Locate every Plasmodium falciparum-infected red blood cell.
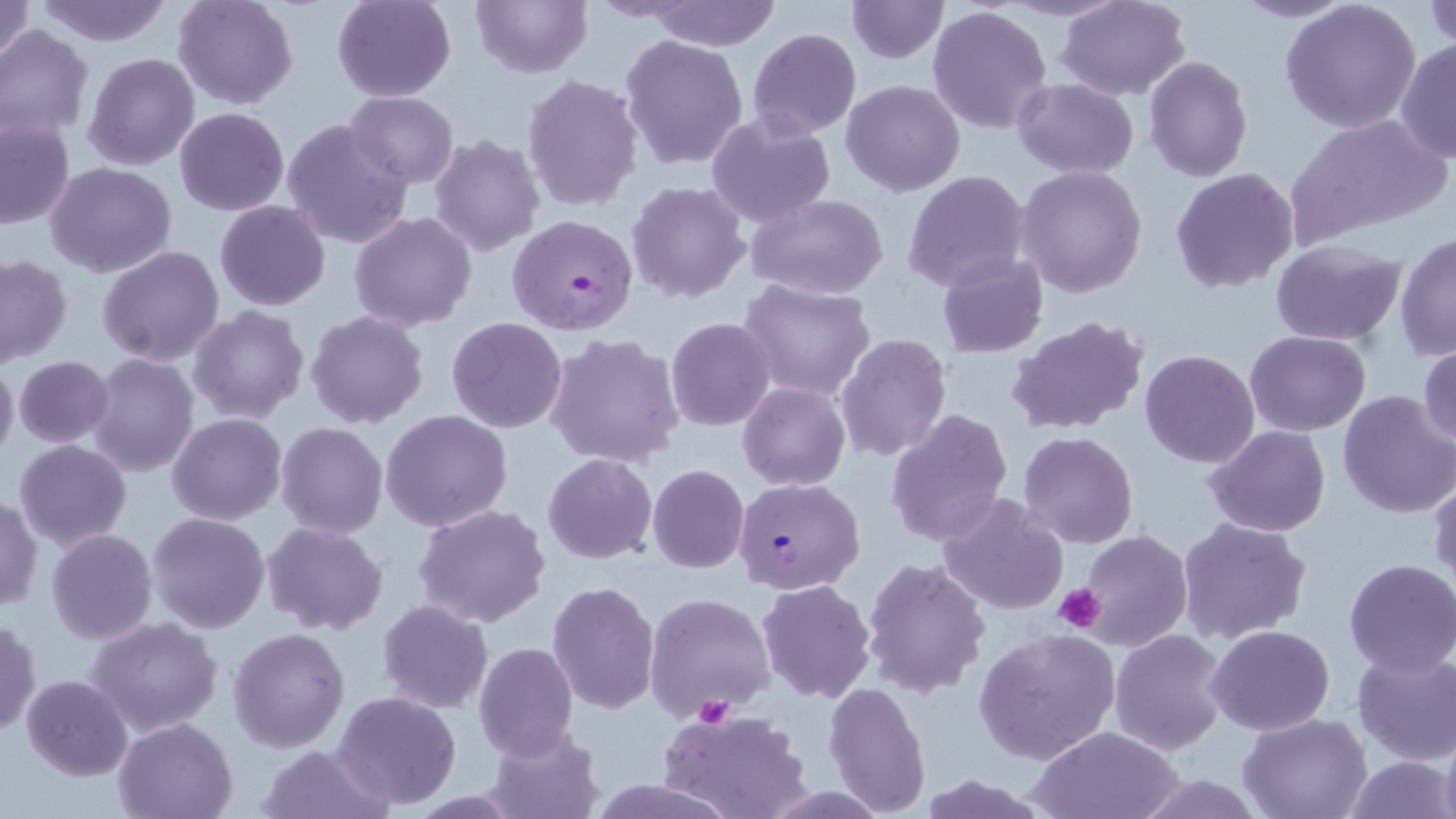

Approximate bounding boxes as named x1/y1/x2/y2 corners in pixels.
Plasmodium falciparum-infected red blood cells: (x1=506, y1=213, x2=638, y2=335), (x1=734, y1=476, x2=866, y2=594).

Platelet locations: (x1=1053, y1=582, x2=1106, y2=633), (x1=695, y1=696, x2=736, y2=728). Uninfected red blood cell locations: (x1=0, y1=0, x2=35, y2=64), (x1=172, y1=0, x2=298, y2=110), (x1=331, y1=0, x2=456, y2=102), (x1=471, y1=0, x2=592, y2=77), (x1=642, y1=0, x2=783, y2=50), (x1=846, y1=0, x2=949, y2=64), (x1=1054, y1=0, x2=1192, y2=101), (x1=1229, y1=0, x2=1356, y2=22), (x1=32, y1=1, x2=176, y2=47), (x1=1280, y1=2, x2=1423, y2=135), (x1=1424, y1=3, x2=1456, y2=51), (x1=926, y1=4, x2=1054, y2=134), (x1=0, y1=24, x2=95, y2=141), (x1=747, y1=28, x2=862, y2=139), (x1=619, y1=35, x2=750, y2=172), (x1=1393, y1=40, x2=1455, y2=161), (x1=81, y1=52, x2=200, y2=171), (x1=1143, y1=55, x2=1253, y2=182), (x1=521, y1=73, x2=643, y2=215), (x1=1012, y1=78, x2=1139, y2=179), (x1=841, y1=80, x2=966, y2=197), (x1=344, y1=90, x2=458, y2=188), (x1=174, y1=107, x2=289, y2=215), (x1=704, y1=114, x2=837, y2=228), (x1=1290, y1=114, x2=1449, y2=240), (x1=0, y1=116, x2=75, y2=230), (x1=282, y1=118, x2=415, y2=249), (x1=429, y1=133, x2=545, y2=256), (x1=45, y1=162, x2=177, y2=279), (x1=1015, y1=165, x2=1148, y2=299), (x1=1169, y1=167, x2=1301, y2=296), (x1=902, y1=170, x2=1031, y2=293), (x1=626, y1=180, x2=751, y2=303), (x1=745, y1=194, x2=890, y2=301), (x1=214, y1=201, x2=331, y2=312), (x1=349, y1=211, x2=477, y2=331), (x1=1394, y1=232, x2=1455, y2=359), (x1=1270, y1=240, x2=1406, y2=347), (x1=96, y1=245, x2=225, y2=367), (x1=0, y1=253, x2=72, y2=367), (x1=936, y1=253, x2=1049, y2=358), (x1=737, y1=279, x2=877, y2=401), (x1=188, y1=305, x2=309, y2=424), (x1=306, y1=310, x2=430, y2=429), (x1=1006, y1=315, x2=1150, y2=436), (x1=445, y1=317, x2=568, y2=434), (x1=666, y1=317, x2=777, y2=432), (x1=1244, y1=331, x2=1371, y2=437), (x1=544, y1=333, x2=687, y2=469), (x1=835, y1=333, x2=954, y2=463), (x1=1418, y1=342, x2=1456, y2=451), (x1=1139, y1=349, x2=1260, y2=468), (x1=84, y1=353, x2=199, y2=478), (x1=12, y1=354, x2=114, y2=448), (x1=0, y1=356, x2=19, y2=466), (x1=738, y1=383, x2=850, y2=490), (x1=1335, y1=389, x2=1456, y2=518), (x1=885, y1=407, x2=1014, y2=548), (x1=380, y1=410, x2=514, y2=531), (x1=168, y1=413, x2=287, y2=525), (x1=275, y1=422, x2=389, y2=540), (x1=1203, y1=425, x2=1331, y2=536), (x1=1018, y1=430, x2=1140, y2=549), (x1=13, y1=440, x2=132, y2=551), (x1=543, y1=452, x2=658, y2=564), (x1=647, y1=464, x2=749, y2=574), (x1=1428, y1=471, x2=1456, y2=592), (x1=937, y1=493, x2=1069, y2=615), (x1=0, y1=494, x2=42, y2=612), (x1=413, y1=504, x2=551, y2=627), (x1=147, y1=512, x2=270, y2=633), (x1=1177, y1=518, x2=1312, y2=644), (x1=261, y1=521, x2=388, y2=635), (x1=45, y1=529, x2=157, y2=644), (x1=1079, y1=530, x2=1192, y2=649), (x1=862, y1=558, x2=991, y2=698), (x1=1341, y1=558, x2=1456, y2=676), (x1=757, y1=578, x2=877, y2=703), (x1=547, y1=580, x2=661, y2=715), (x1=645, y1=590, x2=777, y2=724), (x1=376, y1=600, x2=492, y2=714), (x1=85, y1=616, x2=222, y2=737), (x1=1, y1=618, x2=40, y2=735), (x1=1205, y1=624, x2=1335, y2=735), (x1=227, y1=626, x2=349, y2=753), (x1=974, y1=627, x2=1120, y2=764), (x1=1109, y1=627, x2=1230, y2=756), (x1=473, y1=642, x2=579, y2=759), (x1=1351, y1=649, x2=1456, y2=765), (x1=22, y1=674, x2=132, y2=780), (x1=822, y1=682, x2=933, y2=816), (x1=331, y1=691, x2=462, y2=810), (x1=658, y1=708, x2=810, y2=819), (x1=1237, y1=713, x2=1372, y2=819), (x1=113, y1=716, x2=238, y2=819), (x1=483, y1=721, x2=603, y2=819), (x1=1024, y1=726, x2=1185, y2=819), (x1=1440, y1=726, x2=1456, y2=819), (x1=256, y1=744, x2=393, y2=819), (x1=1343, y1=754, x2=1453, y2=819), (x1=1133, y1=774, x2=1267, y2=818). Slide-level diagnosis: Plasmodium falciparum. 1000x magnification. Thin blood smear. May-Grünwald-Giemsa stain. Optical microscopy. Image is 1456×819 pixels. One field of a larger specimen.